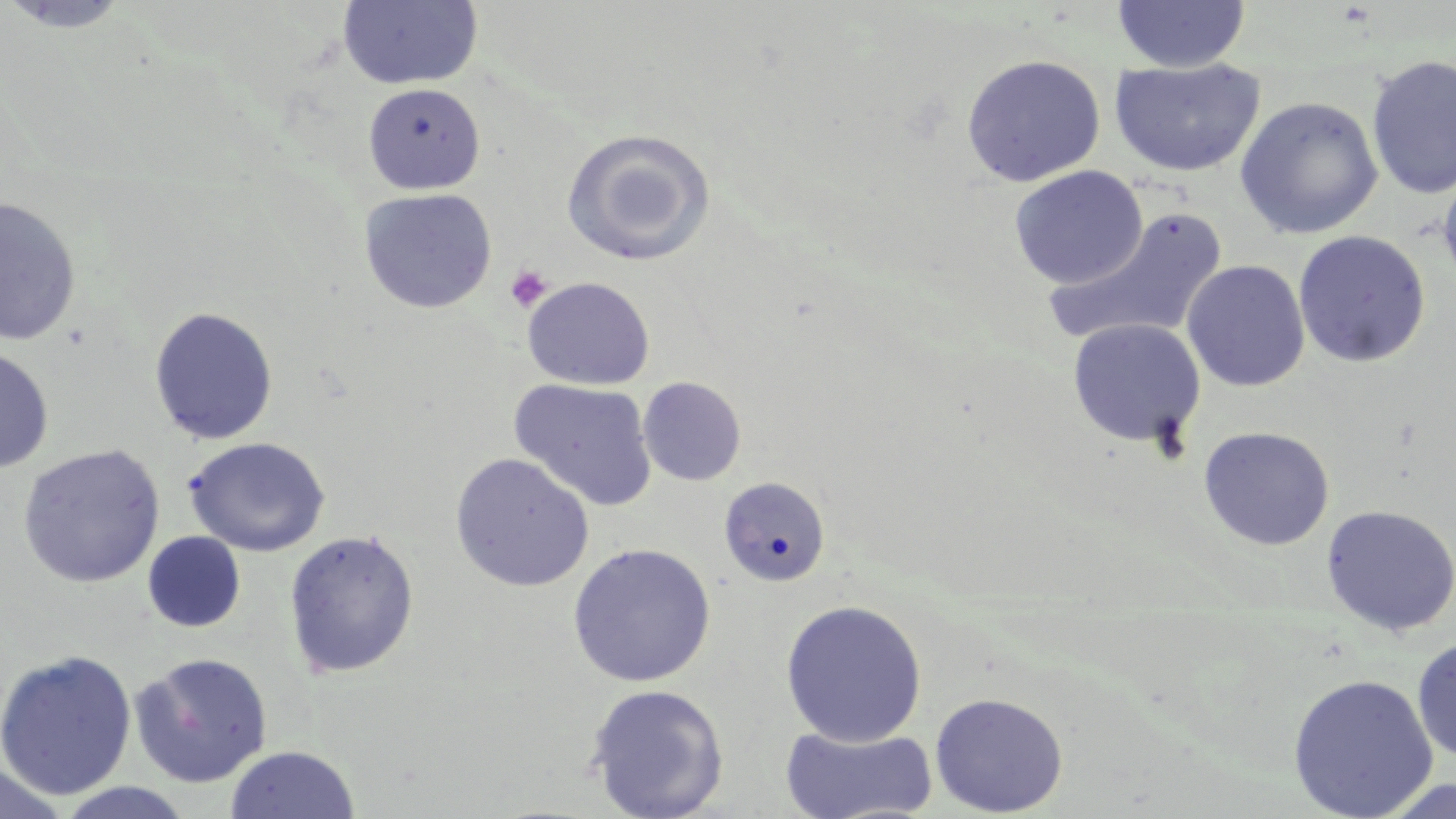

slide-level diagnosis = negative for blood parasites
uninfected red blood cell locations = approximate bounding boxes as [x1, y1, x2, y2] in pixels: [337, 0, 484, 91], [0, 1, 134, 34], [1112, 1, 1250, 73], [960, 54, 1105, 187], [1366, 55, 1456, 200], [1108, 58, 1265, 177], [363, 83, 486, 195], [1234, 96, 1383, 240], [562, 129, 715, 266], [1437, 157, 1456, 295], [1008, 165, 1147, 289], [358, 187, 497, 314], [0, 195, 81, 346], [1041, 208, 1228, 350], [1293, 230, 1431, 367], [1181, 259, 1310, 393], [522, 277, 654, 390], [148, 306, 279, 446], [1067, 318, 1207, 449], [0, 345, 54, 474], [637, 377, 746, 485], [508, 378, 658, 511], [1198, 426, 1335, 551], [182, 436, 330, 557], [18, 444, 165, 588], [450, 452, 594, 592], [718, 476, 831, 587], [1321, 504, 1456, 637], [283, 529, 419, 679], [142, 531, 246, 633], [567, 543, 716, 688], [780, 599, 928, 747], [1412, 635, 1456, 764], [0, 649, 137, 800], [129, 652, 273, 787], [1288, 673, 1438, 818], [585, 683, 729, 819], [929, 691, 1069, 817], [779, 724, 938, 819], [223, 745, 360, 819], [0, 762, 71, 817], [1378, 779, 1456, 818]
magnification = 1000x
stain = May-Grünwald-Giemsa
platelet locations = approximate bounding boxes as [x1, y1, x2, y2] in pixels: [505, 265, 552, 313]
image size = 1456×819 pixels
modality = light microscopy
preparation = thin blood film
field of view = single